Outline each blood parasite and name the species.
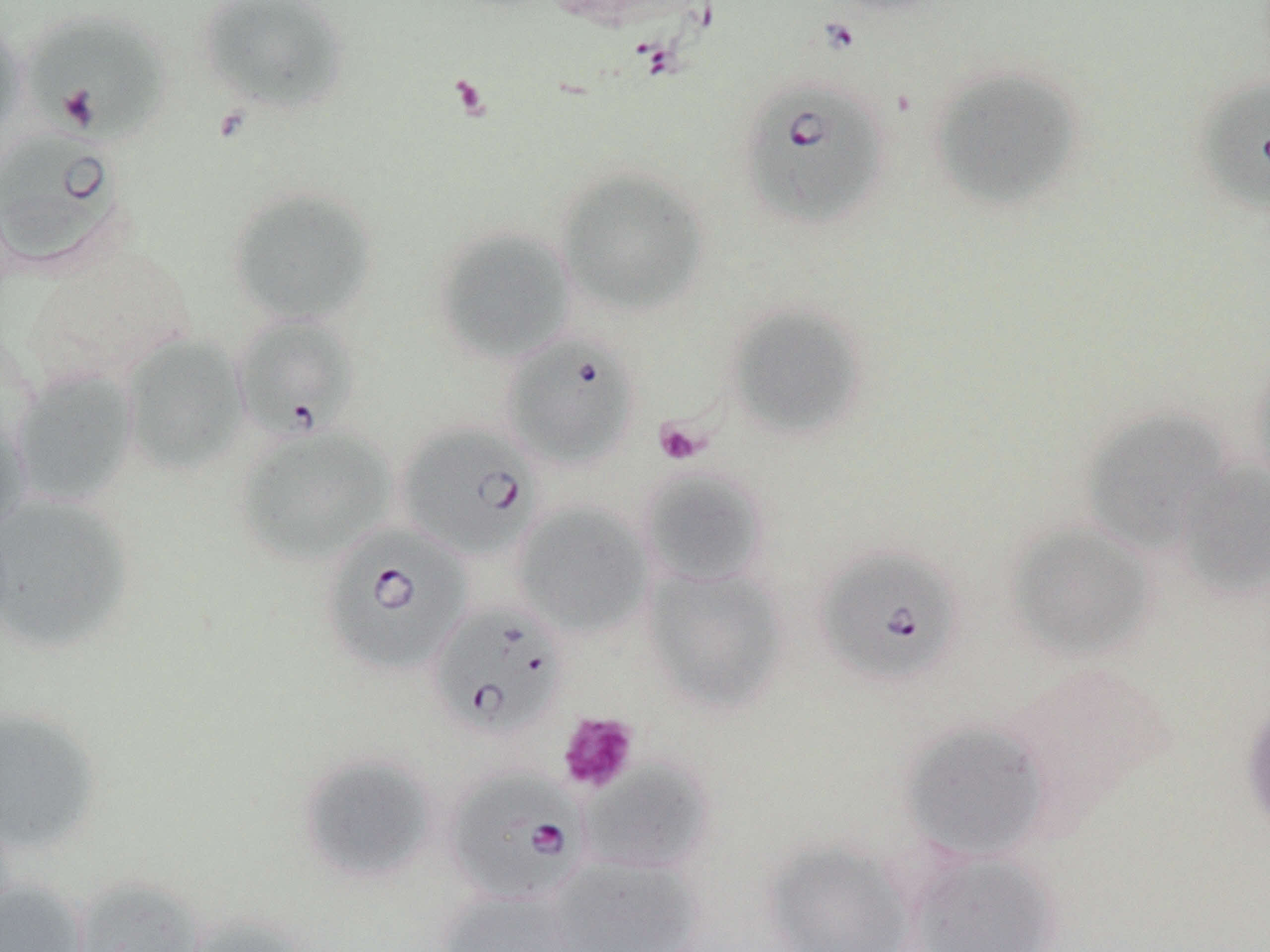
Approximate bounding boxes as named x1/y1/x2/y2 corners in pixels.
Babesia divergens-infected red blood cells: (x1=20, y1=10, x2=173, y2=146), (x1=739, y1=77, x2=891, y2=230), (x1=1198, y1=78, x2=1270, y2=215), (x1=0, y1=129, x2=129, y2=273), (x1=232, y1=314, x2=359, y2=443), (x1=502, y1=333, x2=639, y2=468), (x1=396, y1=422, x2=543, y2=560), (x1=319, y1=523, x2=472, y2=677), (x1=815, y1=544, x2=964, y2=687), (x1=427, y1=599, x2=571, y2=741), (x1=444, y1=769, x2=588, y2=906).
No Plasmodium falciparum, Plasmodium ovale, Plasmodium malariae, Plasmodium vivax, or Trypanosoma brucei observed.

Platelet locations: (x1=654, y1=418, x2=710, y2=466), (x1=557, y1=712, x2=639, y2=795). Uninfected red blood cell locations: (x1=196, y1=0, x2=352, y2=116), (x1=0, y1=15, x2=27, y2=142), (x1=928, y1=65, x2=1082, y2=210), (x1=557, y1=168, x2=707, y2=316), (x1=225, y1=187, x2=378, y2=326), (x1=432, y1=225, x2=577, y2=364), (x1=726, y1=303, x2=868, y2=440), (x1=121, y1=333, x2=248, y2=477), (x1=1246, y1=352, x2=1270, y2=495), (x1=9, y1=367, x2=140, y2=507), (x1=1080, y1=405, x2=1236, y2=555), (x1=0, y1=411, x2=33, y2=543), (x1=235, y1=425, x2=396, y2=565), (x1=1172, y1=460, x2=1270, y2=600), (x1=639, y1=467, x2=770, y2=588), (x1=0, y1=493, x2=136, y2=655), (x1=513, y1=502, x2=653, y2=638), (x1=1005, y1=520, x2=1156, y2=662), (x1=641, y1=566, x2=789, y2=714), (x1=1240, y1=694, x2=1270, y2=840), (x1=0, y1=705, x2=105, y2=856), (x1=897, y1=717, x2=1052, y2=863), (x1=297, y1=751, x2=439, y2=884), (x1=578, y1=758, x2=715, y2=876), (x1=761, y1=836, x2=920, y2=952), (x1=901, y1=848, x2=1062, y2=952), (x1=545, y1=857, x2=703, y2=952), (x1=69, y1=875, x2=209, y2=952), (x1=0, y1=878, x2=89, y2=952), (x1=434, y1=887, x2=584, y2=952), (x1=180, y1=912, x2=312, y2=952). Slide-level diagnosis: Babesia divergens. Image is 1270×952 pixels. Thin blood smear. One field of a larger specimen. Optical microscopy. Captured at 1000x magnification. May-Grünwald-Giemsa-stained preparation.